Evaluate for malaria.
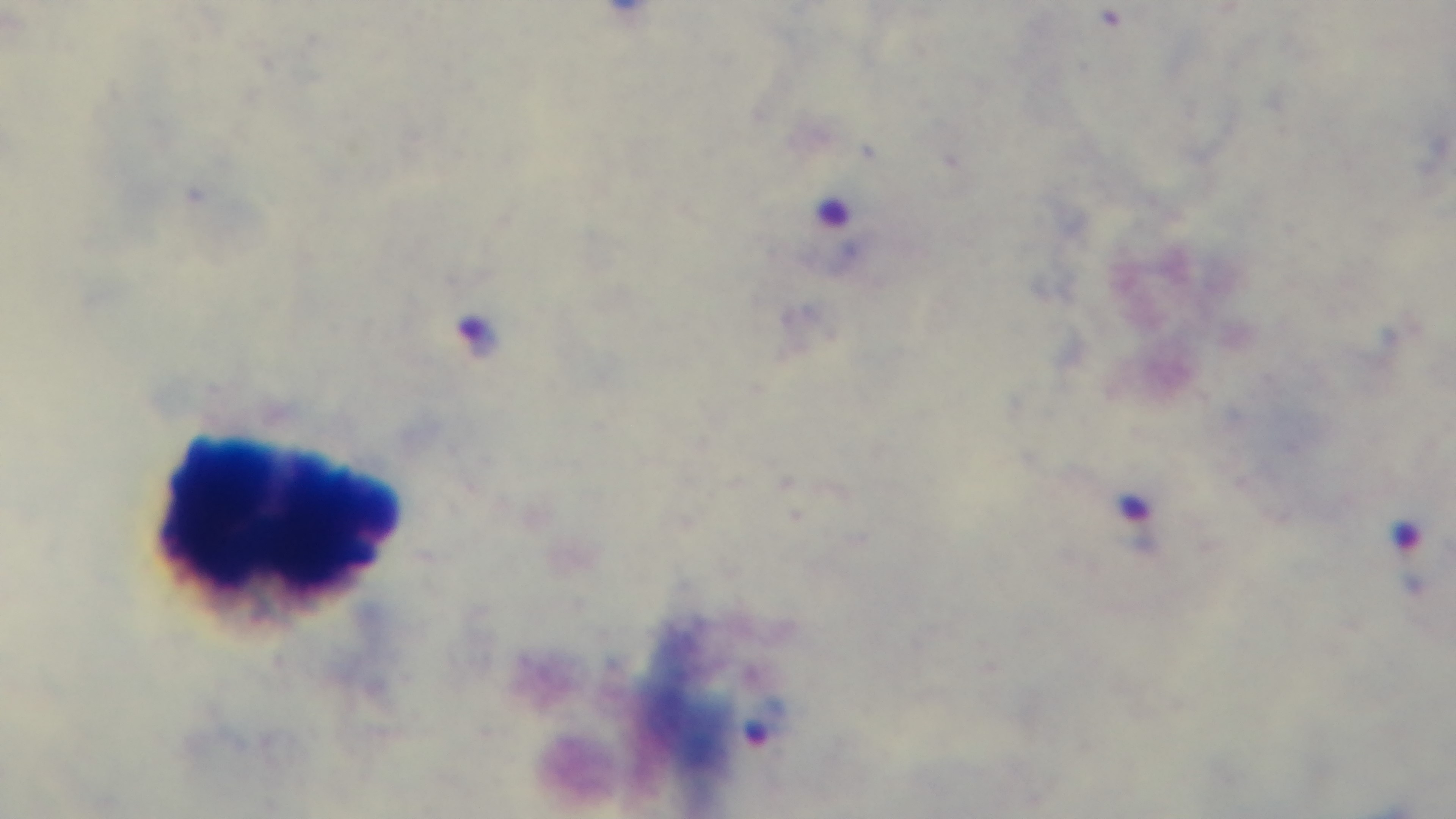
Infected.

preparation: thick
stain: Giemsa
capture: mounted 4K digital camera
field_of_view: single
objective: 100x oil immersion
modality: light microscopy